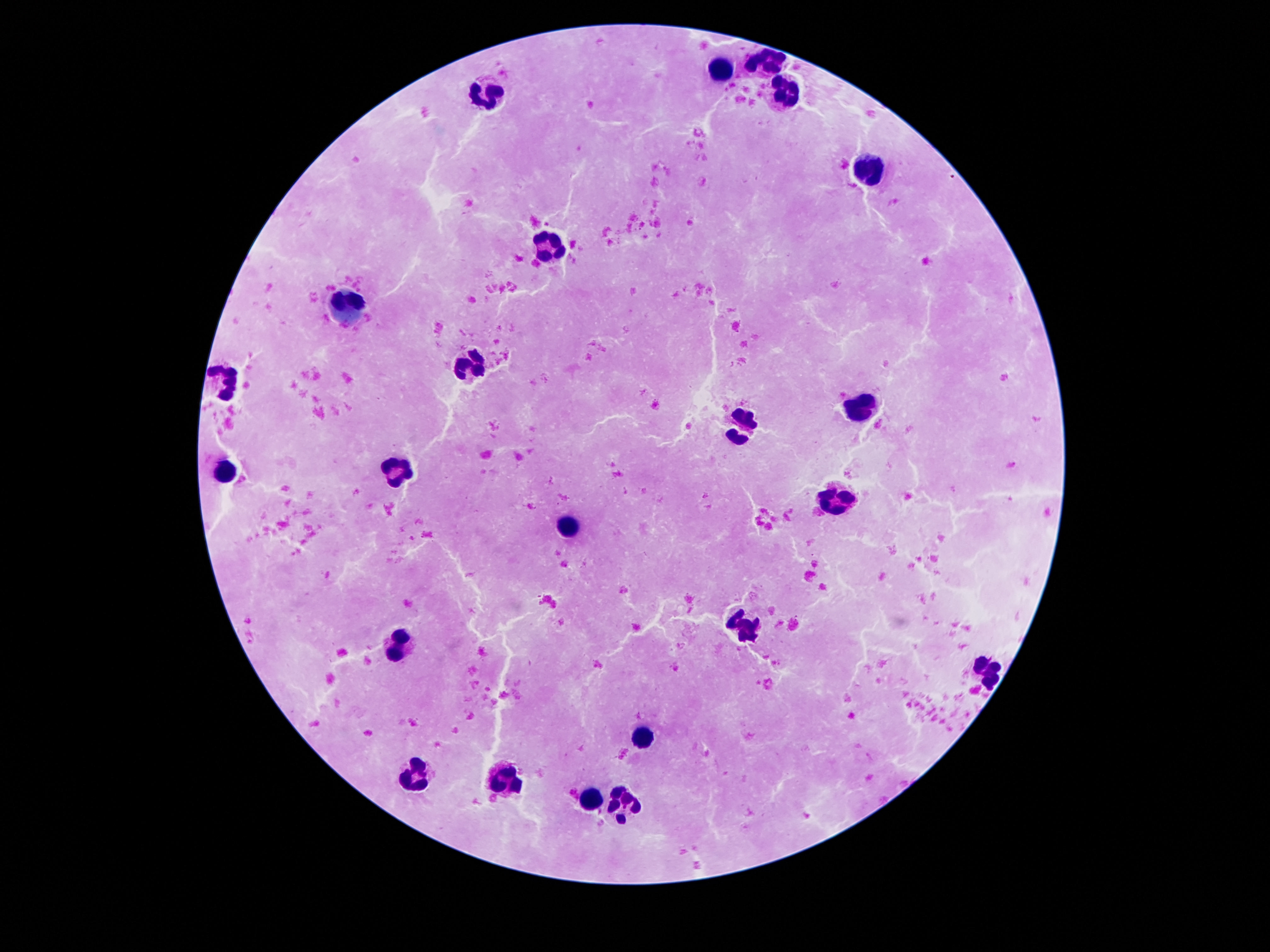
Approximate object centers, in pixels from the top-left corner.
Summary:
  - Leukocyte locations: (x=772, y=62), (x=718, y=70), (x=484, y=91), (x=785, y=93), (x=869, y=167), (x=543, y=249), (x=348, y=304), (x=474, y=366), (x=222, y=381), (x=862, y=409), (x=743, y=425), (x=226, y=469), (x=396, y=473), (x=839, y=501), (x=568, y=525), (x=743, y=626), (x=398, y=642), (x=984, y=672), (x=642, y=736), (x=505, y=775), (x=415, y=776), (x=589, y=800), (x=623, y=805)
  - Capture: smartphone camera through the microscope eyepiece
  - Stain: Giemsa
  - Field of view: single
  - Magnification: 100x
  - Patient malaria status: not infected
  - Preparation: thick peripheral-blood smear
  - Image size: 1270×952 pixels